Assess this cell for malaria.
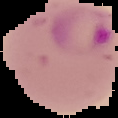
It is parasitized.

The area outside the segmented cell region is set to black. Image is 118×118 pixels. From a thin blood smear.